Classify this cell by malaria status.
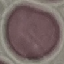
It is uninfected.

preparation = thin smear
stain = Giemsa
capture = smartphone camera at the microscope eyepiece
image type = automatically extracted cell patch, resized to 64 × 64 pixels